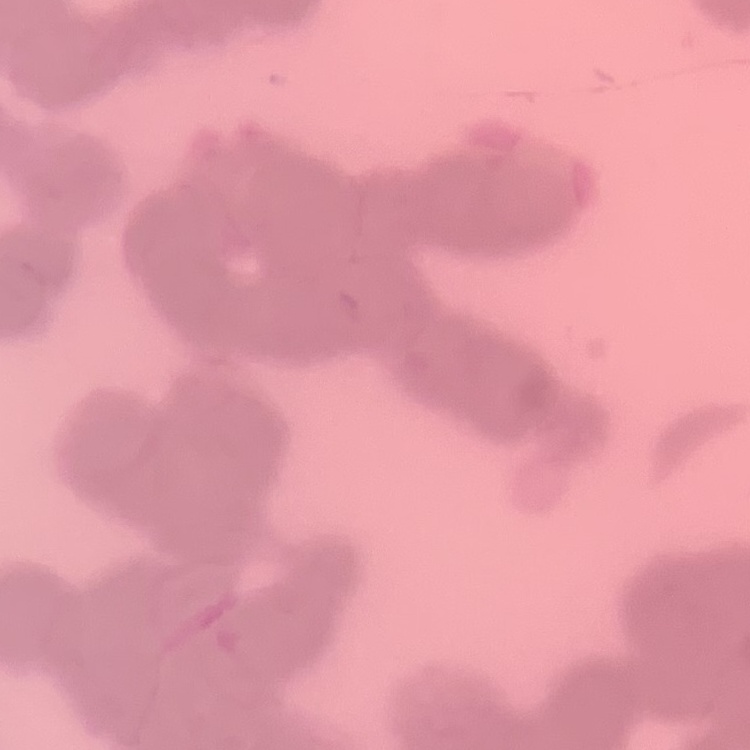
{
  "erythrocyte_morphology": "rouleaux formation",
  "preparation": "thin blood film",
  "image_type": "square crop of a larger photomicrograph",
  "stain": "Field's or Giemsa"
}